Classify this cell by malaria status.
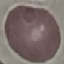

It is uninfected.

image type = cell patch, automatically extracted from a larger field of view and resized to 64 × 64 pixels
capture = smartphone through the microscope eyepiece
stain = Giemsa
preparation = thin blood film